Look for parasitized red blood cells.
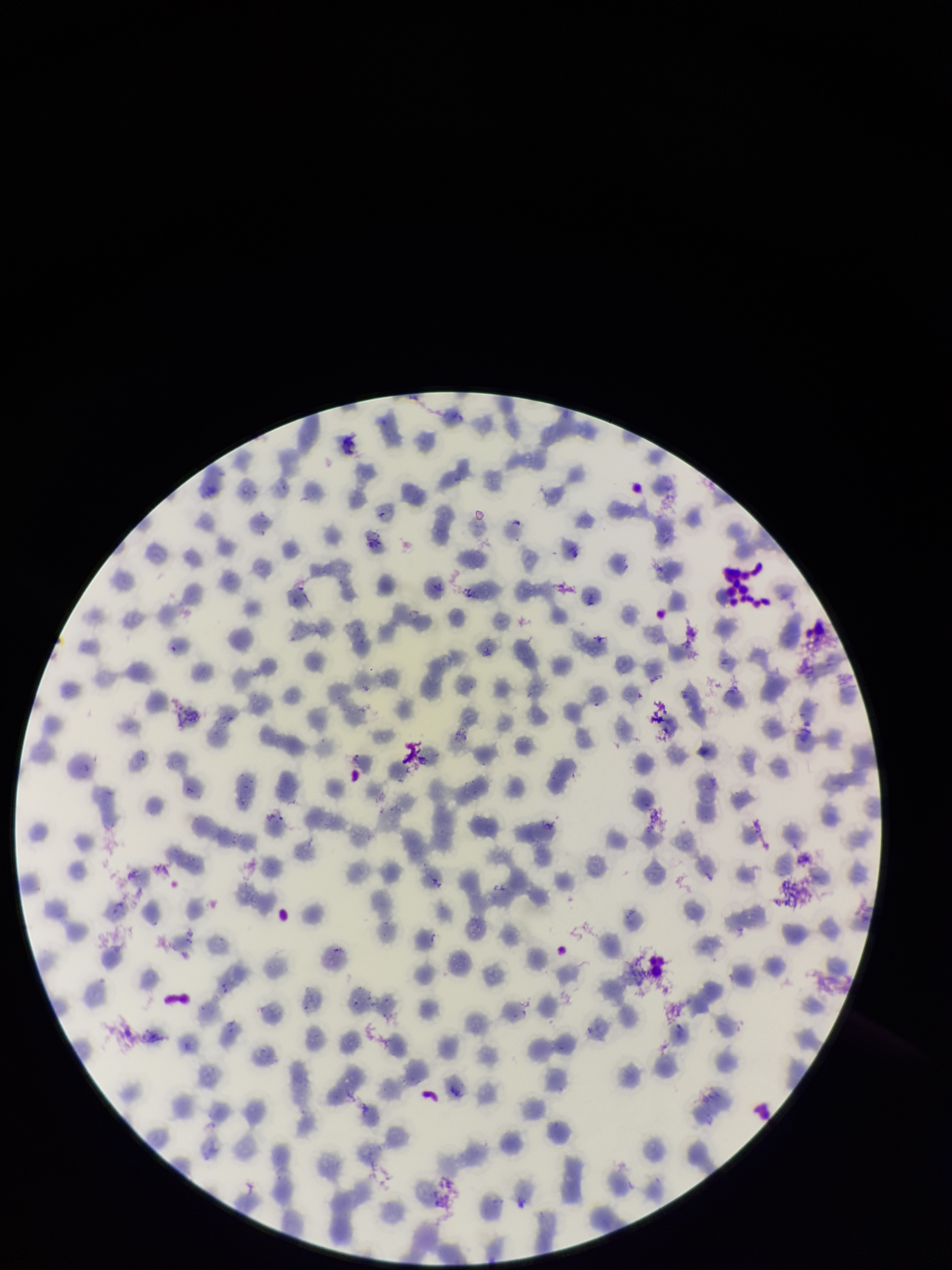
None identified.

species_reported_for_this_patient: Plasmodium falciparum
patient_malaria_status: infected
image_size: 952×1270 pixels
red_blood_cell_count: 215
preparation: thin smear
capture: smartphone photograph through the microscope eyepiece
stain: Giemsa
parasitized_red_blood_cell_count: 0
field_of_view: single